State which cell type is depicted.
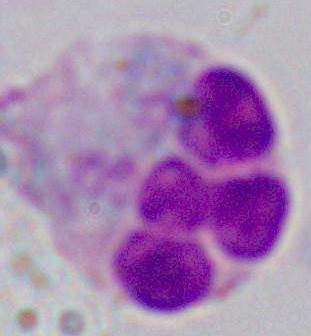

This is a leukocyte.

Captured at 1000x magnification. Photomicrograph.